Assess the morphology of the red blood cells.
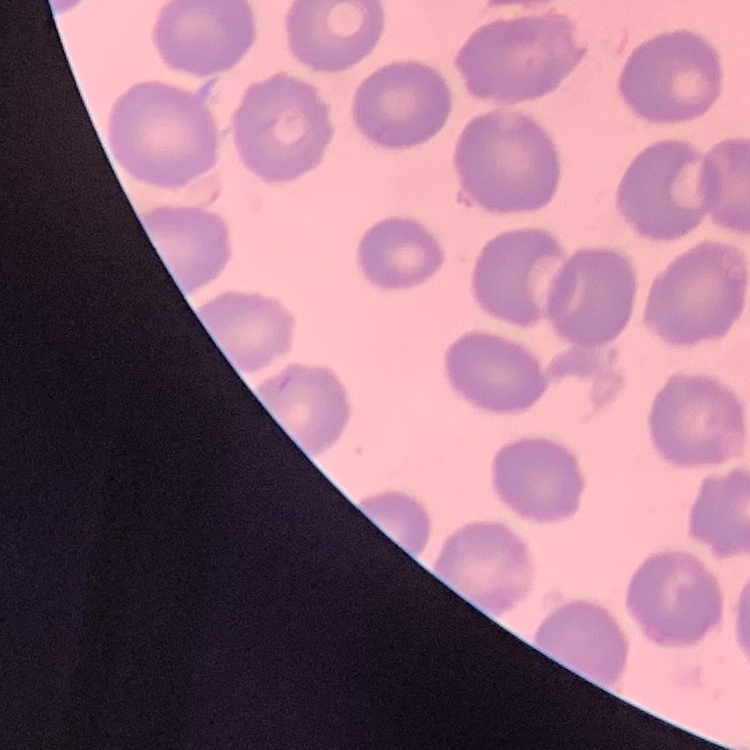

They show no rouleaux formation.

Square crop of a larger photomicrograph. Stained with either Field's or Giemsa. Thin blood film.